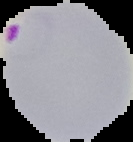
Summary:
  - Image size: 133×142 pixels
  - Image type: segmented cell region with the area outside set to black
  - Malaria status: parasitized
  - Preparation: thin blood smear